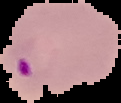

Summary:
  - Preparation: thin blood smear
  - Result: malaria parasites detected
  - Image size: 121×103 pixels
  - Image type: segmented cell region on a black background